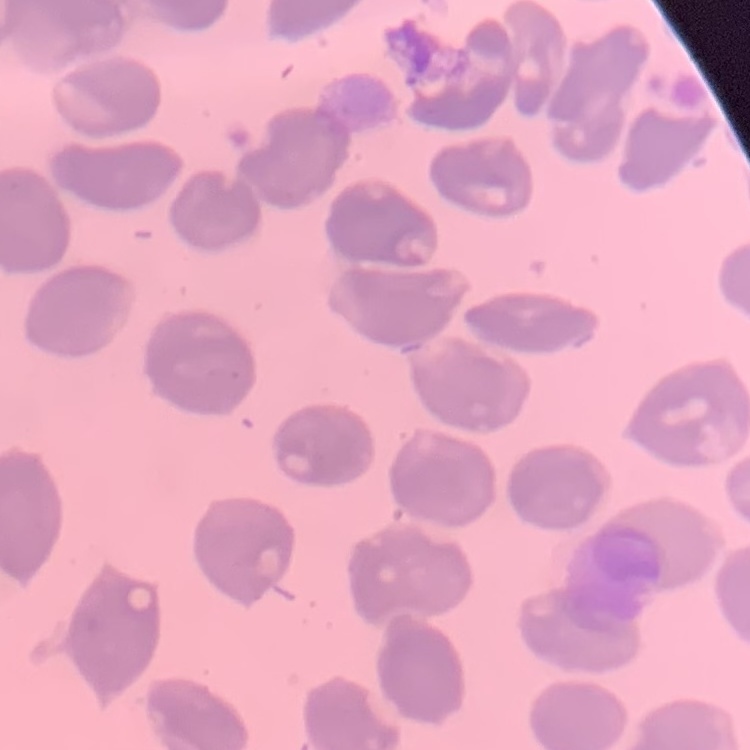

Summary:
  - Erythrocyte morphology: no rouleaux formation
  - Stain: Field's or Giemsa
  - Preparation: thin blood film
  - Image type: one tile cut from a larger photomicrograph